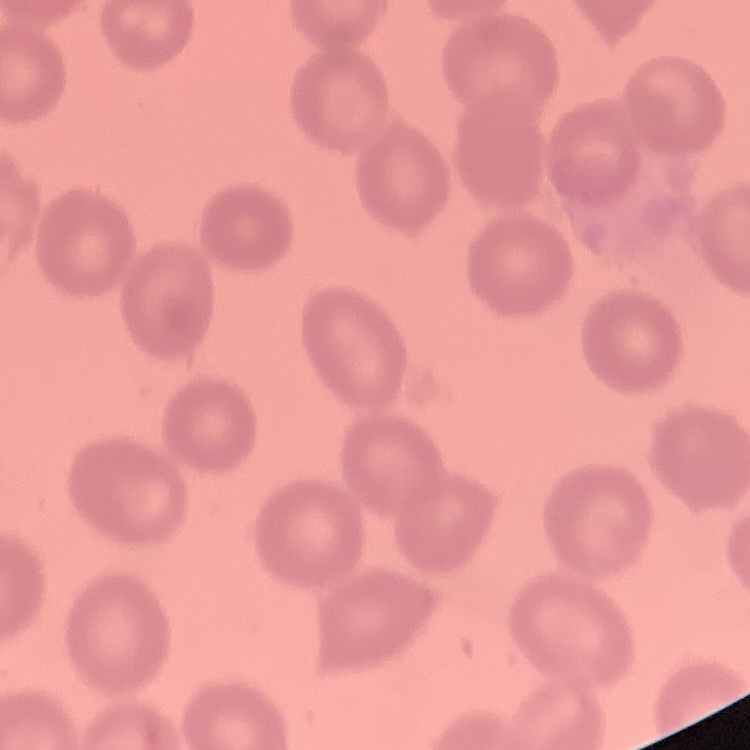

erythrocyte morphology = no rouleaux formation
preparation = thin blood smear
image type = square crop of a larger photomicrograph
stain = Field's or Giemsa